Assess this cell for malaria.
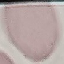
It is uninfected.

stain: Giemsa
preparation: thin blood smear
capture: smartphone through the microscope eyepiece
image_type: cell patch, automatically extracted from a larger field of view and resized to 64 × 64 pixels